Classify this cell by malaria status.
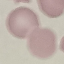

Uninfected.

Summary:
  - Image type: cell patch, automatically extracted from a larger field of view and resized to 64 × 64 pixels
  - Stain: Giemsa
  - Capture: smartphone camera at the microscope eyepiece
  - Preparation: thin blood film